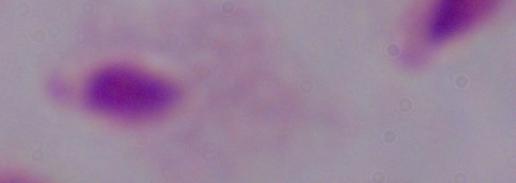
Summary:
  - Modality: micrograph
  - Identification: trichomonad
  - Magnification: 1000x